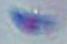

identification = Toxoplasma gondii
magnification = 1000x
modality = photomicrograph